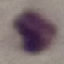

result = negative for malaria parasites
preparation = thin smear
stain = Giemsa
capture = smartphone through the microscope eyepiece
image type = cell patch, automatically extracted from a larger field of view and resized to 64 × 64 pixels